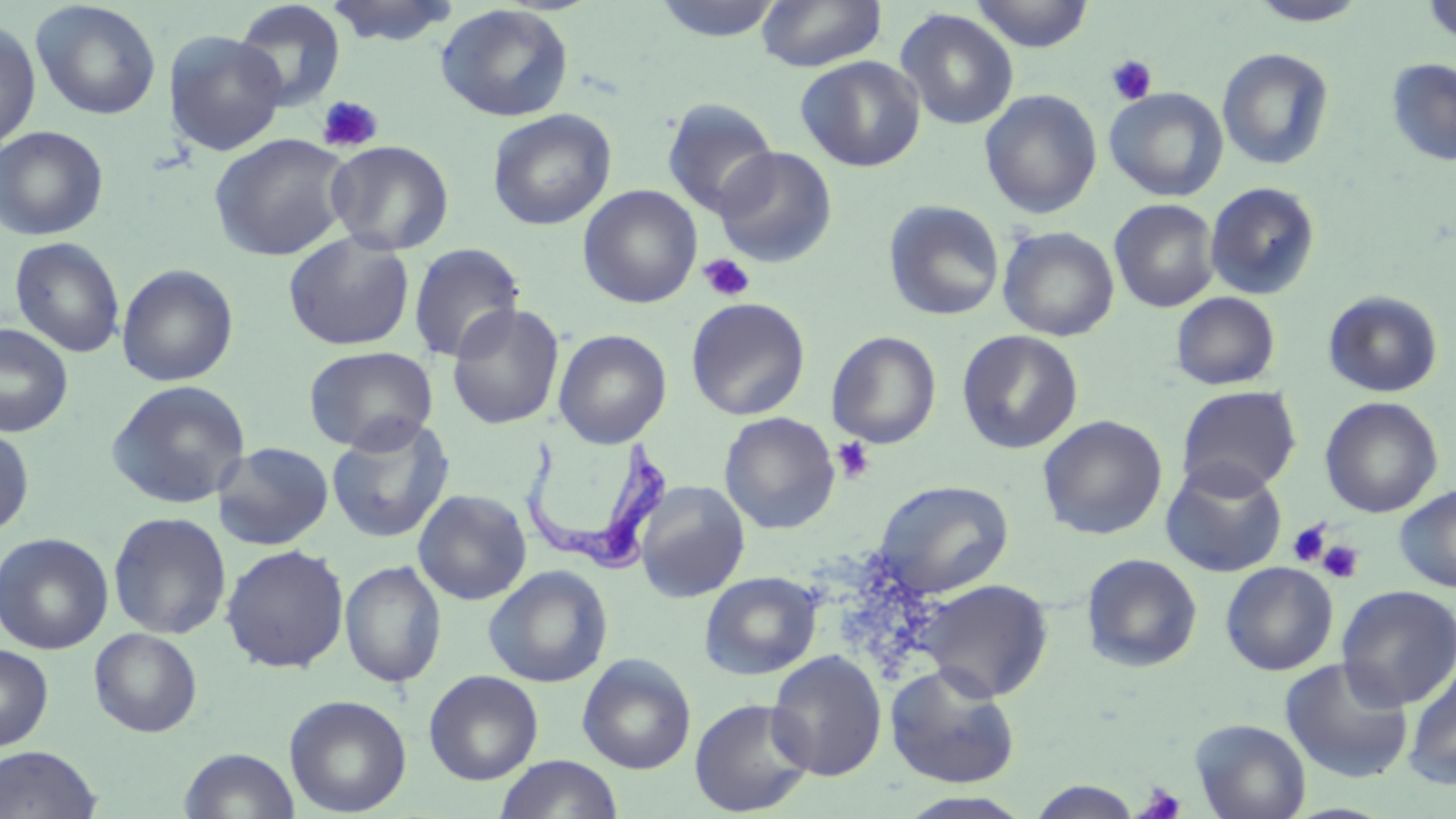

Approximate bounding boxes as named x1/y1/x2/y2 corners in pixels. Platelet locations: (x1=1106, y1=55, x2=1157, y2=106), (x1=316, y1=95, x2=384, y2=154), (x1=698, y1=253, x2=756, y2=302), (x1=832, y1=437, x2=876, y2=483), (x1=1287, y1=520, x2=1331, y2=568), (x1=1318, y1=539, x2=1363, y2=583), (x1=1136, y1=784, x2=1186, y2=818). Trypanosoma brucei locations: (x1=520, y1=429, x2=677, y2=576). Uninfected red blood cell locations: (x1=325, y1=0, x2=459, y2=47), (x1=650, y1=0, x2=785, y2=42), (x1=968, y1=0, x2=1094, y2=52), (x1=1246, y1=0, x2=1372, y2=27), (x1=1421, y1=0, x2=1456, y2=45), (x1=30, y1=1, x2=162, y2=120), (x1=232, y1=1, x2=347, y2=110), (x1=757, y1=1, x2=886, y2=72), (x1=435, y1=3, x2=575, y2=122), (x1=895, y1=8, x2=1019, y2=130), (x1=0, y1=20, x2=41, y2=151), (x1=164, y1=31, x2=287, y2=156), (x1=1217, y1=47, x2=1335, y2=171), (x1=796, y1=55, x2=925, y2=172), (x1=1386, y1=58, x2=1456, y2=167), (x1=1105, y1=88, x2=1228, y2=202), (x1=980, y1=89, x2=1102, y2=219), (x1=661, y1=98, x2=779, y2=218), (x1=487, y1=108, x2=617, y2=230), (x1=0, y1=125, x2=109, y2=241), (x1=209, y1=133, x2=352, y2=261), (x1=326, y1=139, x2=454, y2=255), (x1=712, y1=146, x2=838, y2=268), (x1=1205, y1=182, x2=1321, y2=300), (x1=578, y1=184, x2=702, y2=308), (x1=1109, y1=198, x2=1220, y2=313), (x1=883, y1=200, x2=1004, y2=322), (x1=998, y1=226, x2=1119, y2=341), (x1=282, y1=231, x2=416, y2=351), (x1=9, y1=236, x2=126, y2=358), (x1=408, y1=242, x2=526, y2=363), (x1=117, y1=263, x2=239, y2=387), (x1=1322, y1=290, x2=1443, y2=398), (x1=1171, y1=291, x2=1281, y2=390), (x1=685, y1=297, x2=811, y2=420), (x1=446, y1=303, x2=565, y2=430), (x1=0, y1=323, x2=73, y2=437), (x1=552, y1=329, x2=672, y2=449), (x1=826, y1=330, x2=942, y2=449), (x1=956, y1=330, x2=1084, y2=454), (x1=303, y1=345, x2=439, y2=454), (x1=106, y1=379, x2=251, y2=509), (x1=1176, y1=385, x2=1301, y2=498), (x1=1320, y1=396, x2=1443, y2=518), (x1=719, y1=412, x2=840, y2=534), (x1=1038, y1=415, x2=1168, y2=540), (x1=326, y1=416, x2=455, y2=544), (x1=0, y1=424, x2=35, y2=538), (x1=213, y1=441, x2=335, y2=550), (x1=1161, y1=459, x2=1288, y2=577), (x1=634, y1=480, x2=751, y2=603), (x1=873, y1=480, x2=1014, y2=598), (x1=1394, y1=484, x2=1456, y2=593), (x1=412, y1=489, x2=532, y2=605), (x1=107, y1=511, x2=232, y2=639), (x1=0, y1=532, x2=113, y2=654), (x1=221, y1=544, x2=350, y2=673), (x1=1081, y1=553, x2=1202, y2=673), (x1=340, y1=560, x2=447, y2=688), (x1=1221, y1=562, x2=1338, y2=675), (x1=484, y1=565, x2=612, y2=688), (x1=699, y1=570, x2=822, y2=680), (x1=917, y1=579, x2=1053, y2=702), (x1=1336, y1=585, x2=1456, y2=710), (x1=89, y1=628, x2=203, y2=737), (x1=0, y1=644, x2=53, y2=750), (x1=766, y1=650, x2=887, y2=781), (x1=577, y1=653, x2=696, y2=774), (x1=1281, y1=657, x2=1414, y2=783), (x1=885, y1=663, x2=1021, y2=789), (x1=1403, y1=664, x2=1456, y2=790), (x1=423, y1=670, x2=543, y2=785), (x1=284, y1=694, x2=411, y2=817), (x1=689, y1=697, x2=816, y2=816), (x1=1190, y1=718, x2=1311, y2=819), (x1=0, y1=745, x2=102, y2=818), (x1=179, y1=747, x2=300, y2=818), (x1=494, y1=754, x2=624, y2=819), (x1=1028, y1=779, x2=1144, y2=818), (x1=897, y1=791, x2=1035, y2=819). Slide-level diagnosis: Trypanosoma brucei. 1000x magnification. Thin blood film. May-Grünwald-Giemsa-stained preparation. Image is 1456×819 pixels. Optical microscopy. One field of a larger specimen.